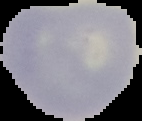

Summary:
  - Preparation: thin blood smear
  - Image type: segmented cell region with the area outside set to black
  - Malaria status: uninfected
  - Image size: 142×121 pixels